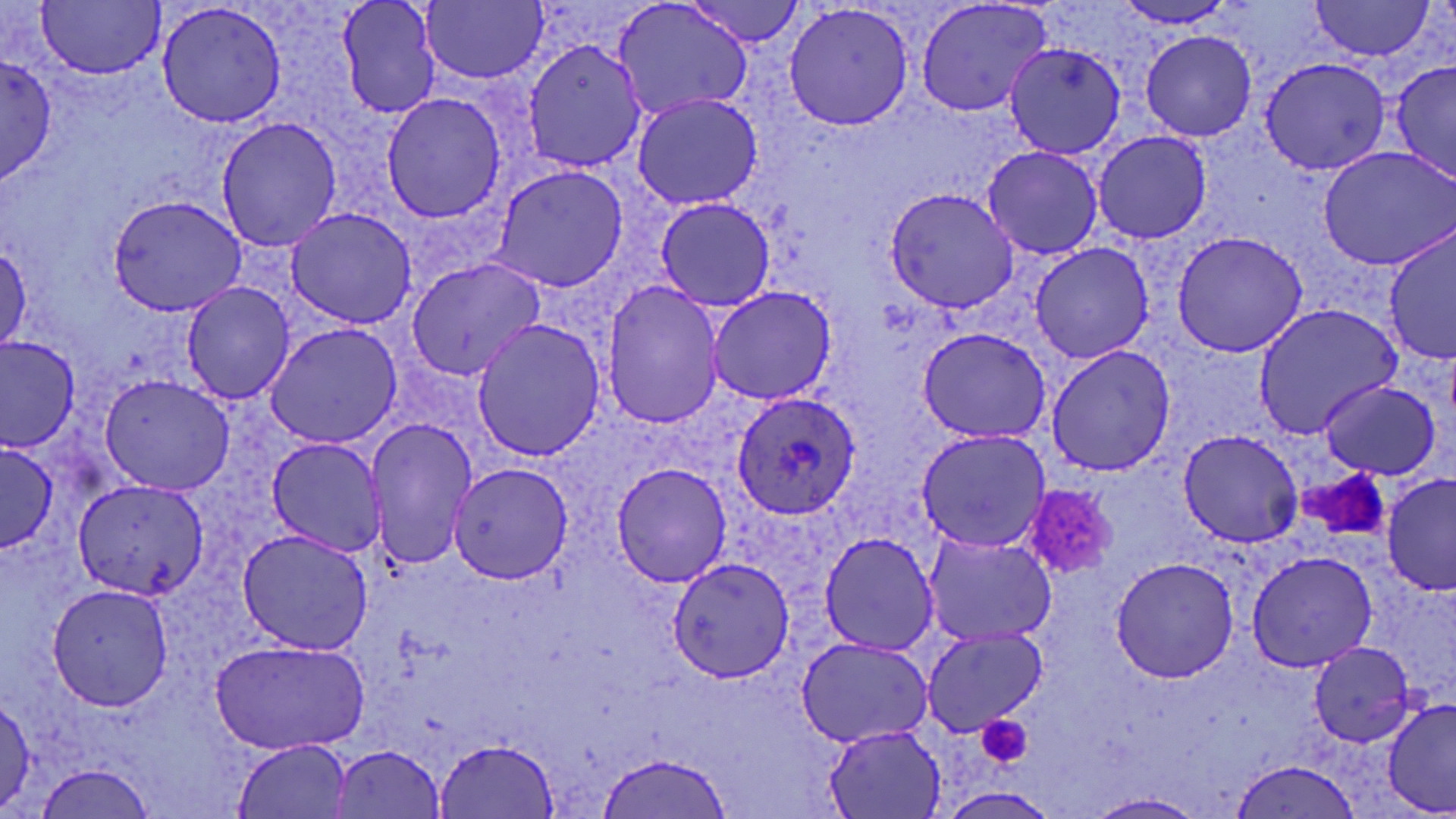

Summary:
  - Coordinate format: approximate bounding boxes as [x1, y1, x2, y2] in pixels
  - Plasmodium ovale-infected red blood cell locations: [729, 391, 863, 522]
  - Platelet locations: [1297, 467, 1388, 537], [1019, 484, 1119, 580], [976, 716, 1032, 769]
  - Uninfected red blood cell locations: [37, 0, 166, 79], [335, 0, 442, 121], [422, 0, 548, 85], [682, 0, 806, 47], [912, 0, 1056, 120], [1306, 0, 1437, 62], [611, 1, 751, 121], [1111, 1, 1248, 30], [154, 3, 290, 130], [783, 5, 916, 130], [1139, 28, 1259, 142], [520, 39, 650, 172], [1006, 41, 1127, 163], [0, 54, 58, 184], [1256, 55, 1394, 175], [1387, 58, 1455, 183], [380, 92, 510, 224], [631, 94, 764, 209], [215, 115, 343, 251], [1091, 130, 1211, 242], [979, 145, 1104, 261], [1317, 146, 1456, 270], [487, 163, 632, 294], [883, 187, 1021, 314], [107, 194, 247, 317], [651, 197, 778, 311], [284, 208, 416, 329], [1384, 225, 1455, 365], [1170, 230, 1311, 358], [1, 241, 30, 354], [1027, 243, 1157, 364], [402, 255, 549, 382], [601, 281, 727, 429], [179, 282, 295, 405], [708, 287, 836, 406], [1251, 303, 1403, 437], [470, 317, 604, 462], [261, 320, 403, 448], [918, 326, 1055, 447], [0, 334, 80, 451], [1045, 343, 1175, 478], [98, 372, 237, 497], [1317, 379, 1445, 481], [360, 417, 480, 569], [916, 427, 1053, 554], [1177, 428, 1306, 548], [265, 435, 387, 558], [0, 441, 59, 552], [609, 462, 733, 588], [448, 464, 575, 584], [1382, 471, 1455, 597], [70, 478, 206, 603], [235, 529, 373, 654], [920, 531, 1058, 645], [816, 532, 941, 655], [1245, 551, 1382, 674], [1109, 556, 1240, 682], [665, 557, 793, 685], [45, 582, 175, 711], [919, 624, 1048, 735], [796, 635, 933, 747], [210, 638, 370, 754], [1307, 642, 1417, 748], [0, 691, 36, 813], [1382, 695, 1456, 818], [821, 722, 949, 817], [233, 737, 354, 817], [434, 738, 562, 818], [326, 745, 448, 817], [597, 752, 735, 817], [1228, 758, 1366, 819], [27, 761, 158, 817], [1083, 792, 1209, 819]
  - Slide-level diagnosis: Plasmodium ovale
  - Magnification: 1000x
  - Field of view: single
  - Stain: May-Grünwald-Giemsa
  - Image size: 1456×819 pixels
  - Preparation: thin blood film
  - Modality: optical microscopy